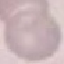

Summary:
  - Malaria status: uninfected
  - Image type: cell patch, automatically extracted from a larger field of view and resized to 64 × 64 pixels
  - Preparation: thin blood smear
  - Capture: smartphone camera at the microscope eyepiece
  - Stain: Giemsa